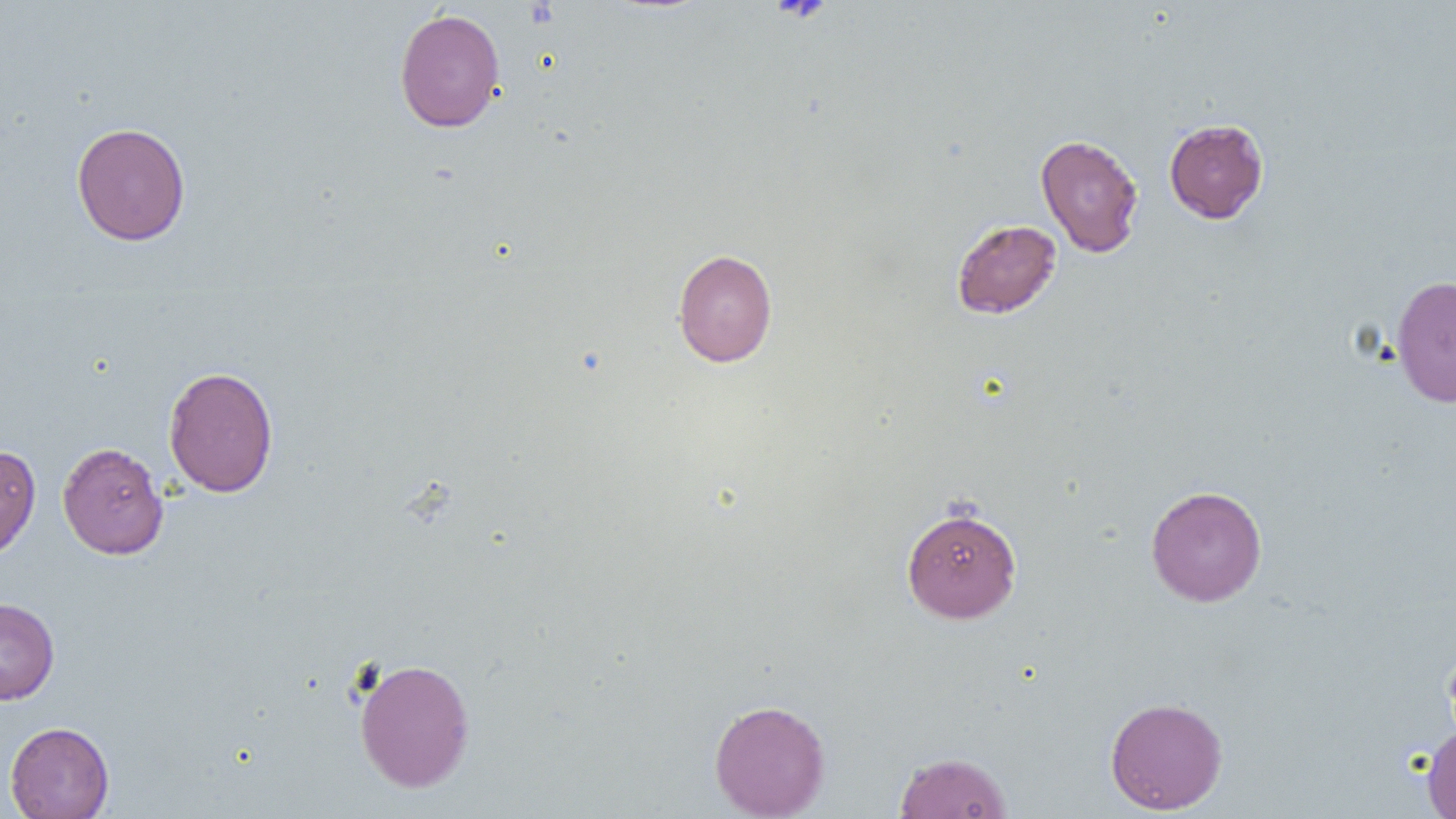

{
  "slide_level_diagnosis": "negative for blood parasites",
  "magnification": "1000x",
  "image_size": "1456×819 pixels",
  "platelet_locations": "approximate bounding boxes as (x1,y1)-(x2,y2) corner pairs in pixels: (771,0)-(833,23)",
  "field_of_view": "one of a larger specimen",
  "preparation": "thin blood film",
  "uninfected_red_blood_cell_locations": "approximate bounding boxes as (x1,y1)-(x2,y2) corner pairs in pixels: (393,8)-(505,133), (1164,118)-(1269,224), (71,121)-(191,246), (1035,133)-(1144,258), (951,219)-(1062,319), (673,248)-(777,367), (1390,274)-(1456,407), (163,366)-(279,497), (57,441)-(169,559), (0,444)-(41,561), (1145,485)-(1268,607), (902,506)-(1022,623), (0,597)-(59,705), (1444,641)-(1456,746), (353,657)-(476,793), (1105,696)-(1228,814), (709,698)-(831,818), (5,721)-(114,819), (1422,726)-(1456,819), (894,751)-(1013,818)",
  "modality": "light microscopy"
}